Identify the parasite.
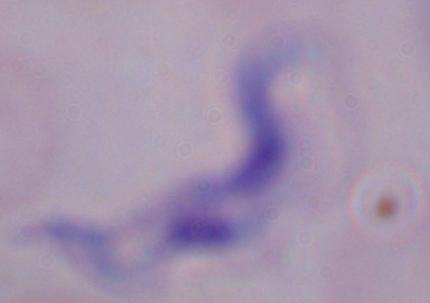
This is a trypanosome.

modality = micrograph
magnification = 1000x